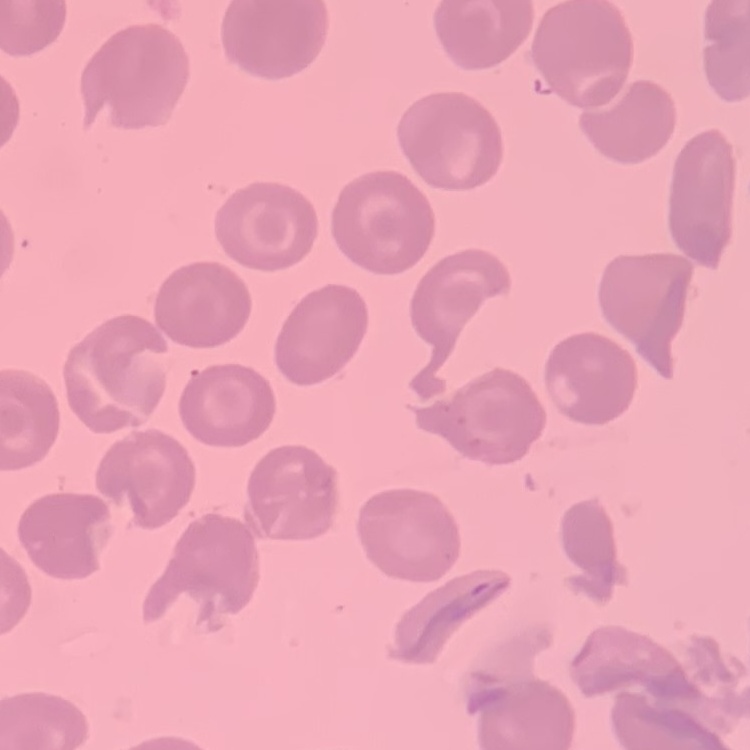

{
  "erythrocyte_morphology": "no rouleaux formation",
  "stain": "Field's or Giemsa",
  "image_type": "one tile cut from a larger photomicrograph",
  "preparation": "thin peripheral smear"
}